Comment on the morphology of the erythrocytes.
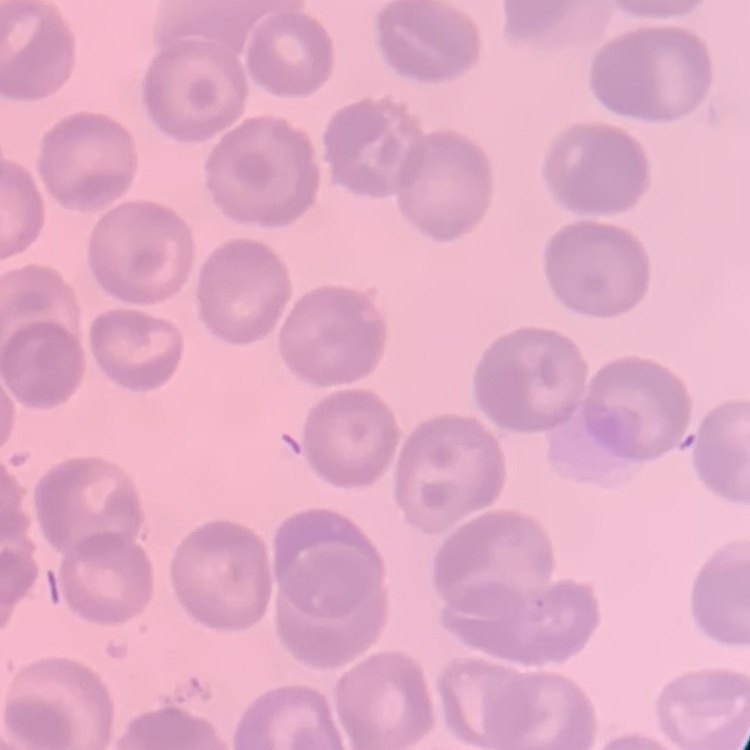

They show no rouleaux formation.

Summary:
  - Stain: Field's or Giemsa
  - Image type: one tile cut from a larger photomicrograph
  - Preparation: thin blood film